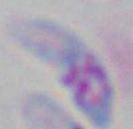 1000x magnification. Toxoplasma gondii is shown. Photomicrograph.